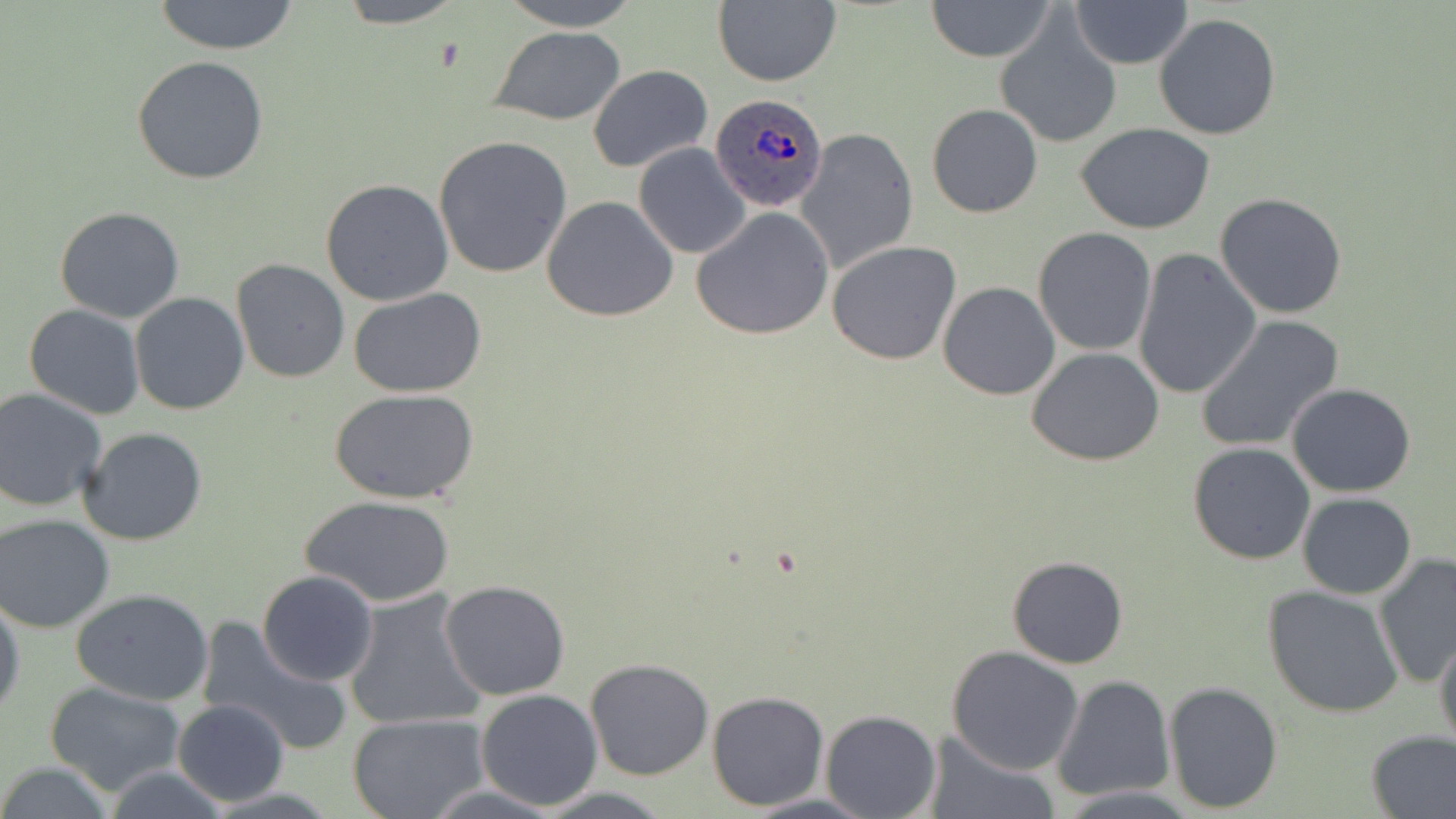

Summary:
  - Coordinate format: approximate bounding boxes as named x1/y1/x2/y2 corners in pixels
  - Plasmodium ovale-infected red blood cell locations: (x1=711, y1=92, x2=828, y2=211)
  - Uninfected red blood cell locations: (x1=149, y1=0, x2=303, y2=54), (x1=331, y1=0, x2=469, y2=28), (x1=498, y1=0, x2=645, y2=30), (x1=924, y1=0, x2=1056, y2=63), (x1=1069, y1=1, x2=1193, y2=69), (x1=713, y1=2, x2=841, y2=87), (x1=996, y1=13, x2=1121, y2=150), (x1=1153, y1=14, x2=1282, y2=140), (x1=488, y1=26, x2=626, y2=125), (x1=132, y1=55, x2=268, y2=184), (x1=587, y1=65, x2=713, y2=172), (x1=927, y1=103, x2=1042, y2=218), (x1=1077, y1=124, x2=1216, y2=234), (x1=797, y1=127, x2=919, y2=272), (x1=433, y1=135, x2=573, y2=278), (x1=633, y1=143, x2=751, y2=259), (x1=321, y1=178, x2=454, y2=307), (x1=1214, y1=193, x2=1349, y2=319), (x1=541, y1=195, x2=679, y2=322), (x1=54, y1=206, x2=185, y2=323), (x1=692, y1=208, x2=835, y2=341), (x1=1033, y1=227, x2=1157, y2=357), (x1=827, y1=240, x2=962, y2=364), (x1=1132, y1=249, x2=1261, y2=401), (x1=231, y1=259, x2=349, y2=383), (x1=937, y1=280, x2=1061, y2=400), (x1=348, y1=286, x2=486, y2=397), (x1=131, y1=293, x2=249, y2=414), (x1=23, y1=305, x2=145, y2=419), (x1=1196, y1=316, x2=1344, y2=454), (x1=1027, y1=345, x2=1165, y2=466), (x1=1287, y1=384, x2=1417, y2=498), (x1=0, y1=387, x2=107, y2=512), (x1=331, y1=387, x2=481, y2=504), (x1=77, y1=426, x2=208, y2=547), (x1=1188, y1=443, x2=1316, y2=565), (x1=1297, y1=491, x2=1417, y2=598), (x1=299, y1=495, x2=455, y2=607), (x1=0, y1=514, x2=116, y2=634), (x1=1373, y1=554, x2=1456, y2=689), (x1=1006, y1=555, x2=1129, y2=668), (x1=257, y1=570, x2=380, y2=689), (x1=439, y1=580, x2=570, y2=701), (x1=1262, y1=585, x2=1405, y2=718), (x1=70, y1=588, x2=214, y2=707), (x1=343, y1=589, x2=488, y2=732), (x1=0, y1=592, x2=25, y2=724), (x1=198, y1=619, x2=350, y2=757), (x1=1433, y1=628, x2=1456, y2=753), (x1=946, y1=645, x2=1084, y2=775), (x1=583, y1=659, x2=714, y2=781), (x1=1053, y1=675, x2=1174, y2=801), (x1=1163, y1=681, x2=1284, y2=813), (x1=43, y1=682, x2=189, y2=797), (x1=474, y1=689, x2=604, y2=812), (x1=706, y1=690, x2=829, y2=811), (x1=172, y1=698, x2=289, y2=805), (x1=821, y1=708, x2=941, y2=818), (x1=348, y1=714, x2=490, y2=819), (x1=1363, y1=729, x2=1456, y2=818), (x1=928, y1=733, x2=1052, y2=819), (x1=0, y1=762, x2=115, y2=818), (x1=99, y1=764, x2=234, y2=819), (x1=1055, y1=787, x2=1201, y2=817), (x1=739, y1=791, x2=880, y2=819)
  - Slide-level diagnosis: Plasmodium ovale
  - Magnification: 1000x
  - Field of view: single
  - Image size: 1456×819 pixels
  - Stain: May-Grünwald-Giemsa
  - Preparation: thin blood film
  - Modality: optical microscopy